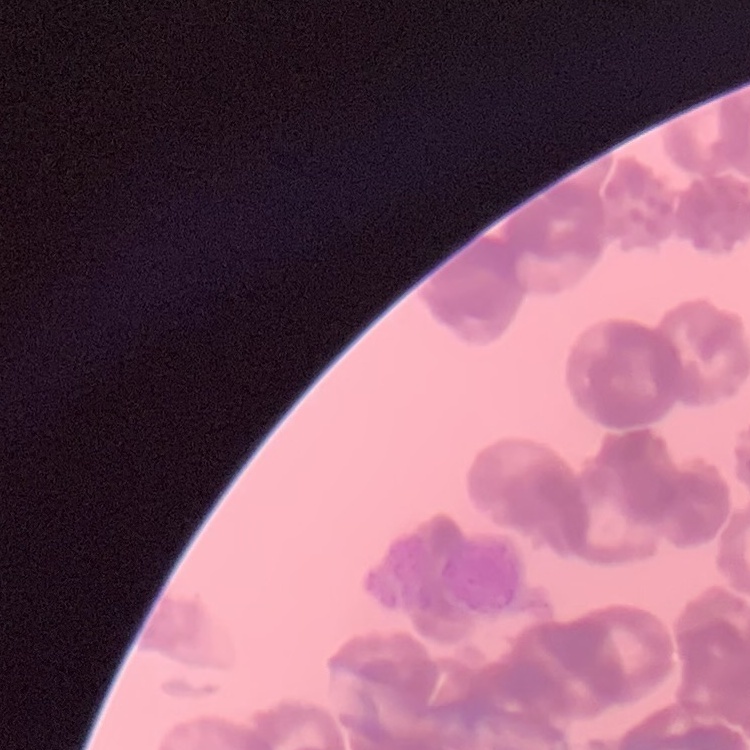

The erythrocytes show rouleaux formation. Field's or Giemsa stain. One tile cut from a larger photomicrograph. Thin blood smear.